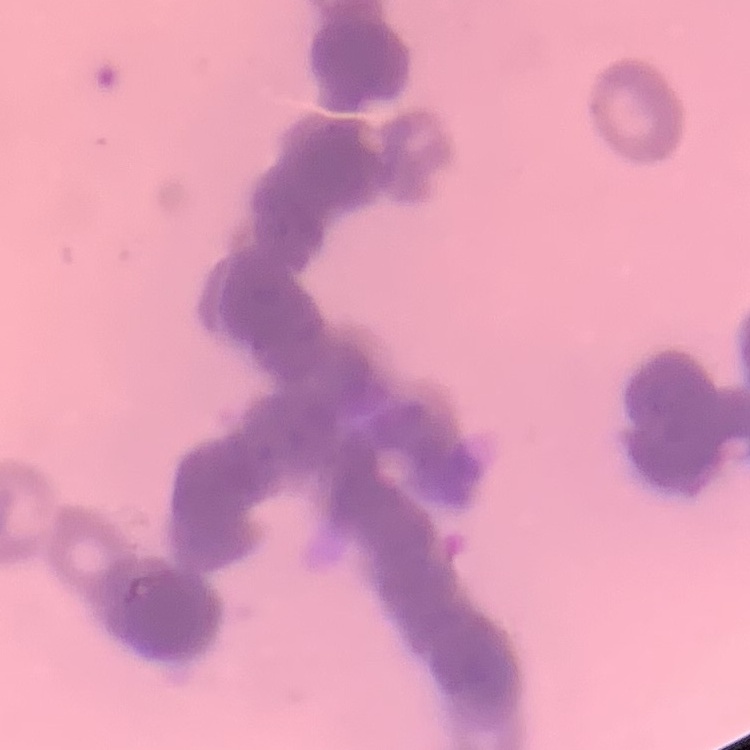

The red blood cells show rouleaux formation. One tile cut from a larger photomicrograph. Field's or Giemsa stain. Thin peripheral smear.